Identify the cell.
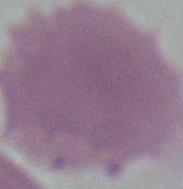
An erythrocyte.

Micrograph. Captured at 1000x magnification.